Look for Plasmodium parasites.
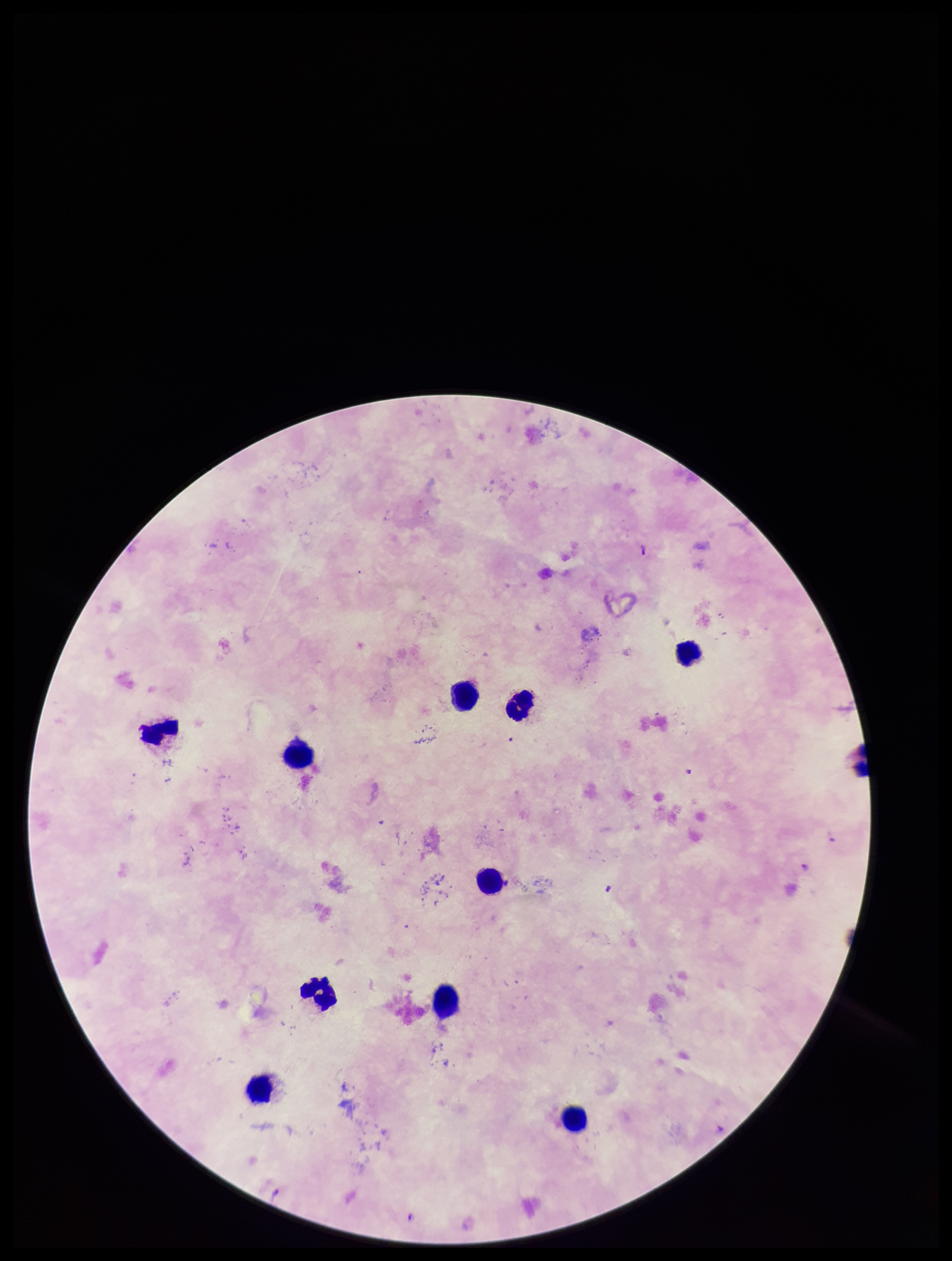
Identified.

patient malaria status = infected
image size = 952×1261 pixels
preparation = thick blood smear
stain = Giemsa
species reported for this patient = Plasmodium falciparum
field of view = single
capture = smartphone photograph through the microscope eyepiece
parasite count = 1
leukocyte count = 10